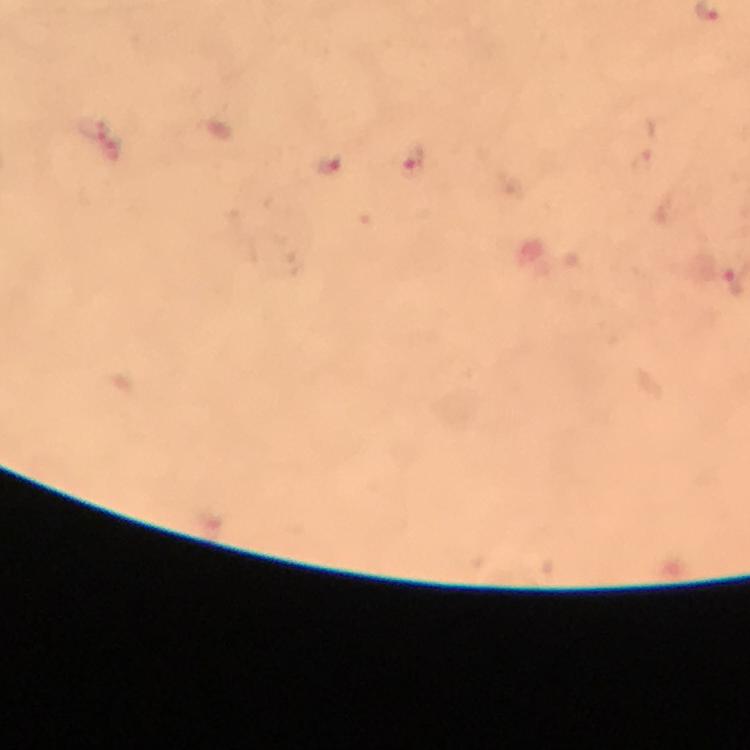
Approximate object centers, in pixels from the top-left corner.
Summary:
  - Plasmodium parasite locations: (x=91, y=128), (x=415, y=164), (x=327, y=166), (x=734, y=282)
  - Immersion oil: used
  - Stain: Giemsa
  - Magnification: 100x
  - Capture: smartphone camera through the microscope
  - Preparation: thick blood film
  - Context: from a diagnostic examination for malaria
  - Image size: 750×750 pixels
  - Cropped from: a single field of view